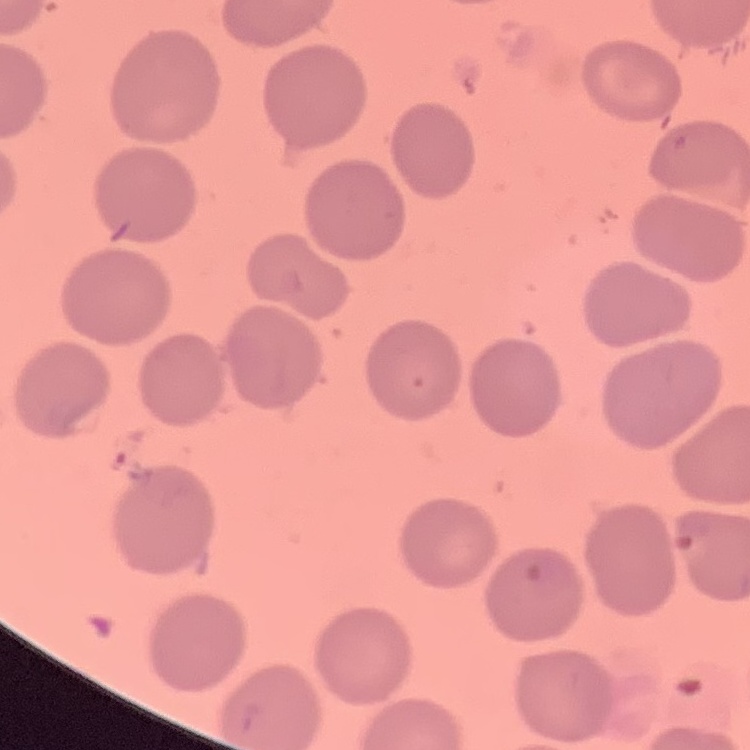
The red blood cells show no rouleaux formation. Field's or Giemsa stain. Square crop of a larger photomicrograph. Thin peripheral smear.